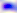 Photomicrograph. Captured at 400x magnification. Toxoplasma gondii is shown.